State which parasite is depicted.
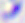

Toxoplasma gondii.

modality = micrograph
magnification = 400x